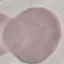

result = no malaria parasites detected
stain = Giemsa
capture = smartphone camera at the microscope eyepiece
image type = automatically extracted cell patch, resized to 64 × 64 pixels
preparation = thin blood smear